Report the malaria status of this cell.
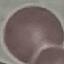

Uninfected.

image type = automatically extracted cell patch, resized to 64 × 64 pixels
stain = Giemsa
preparation = thin blood smear
capture = smartphone camera at the microscope eyepiece